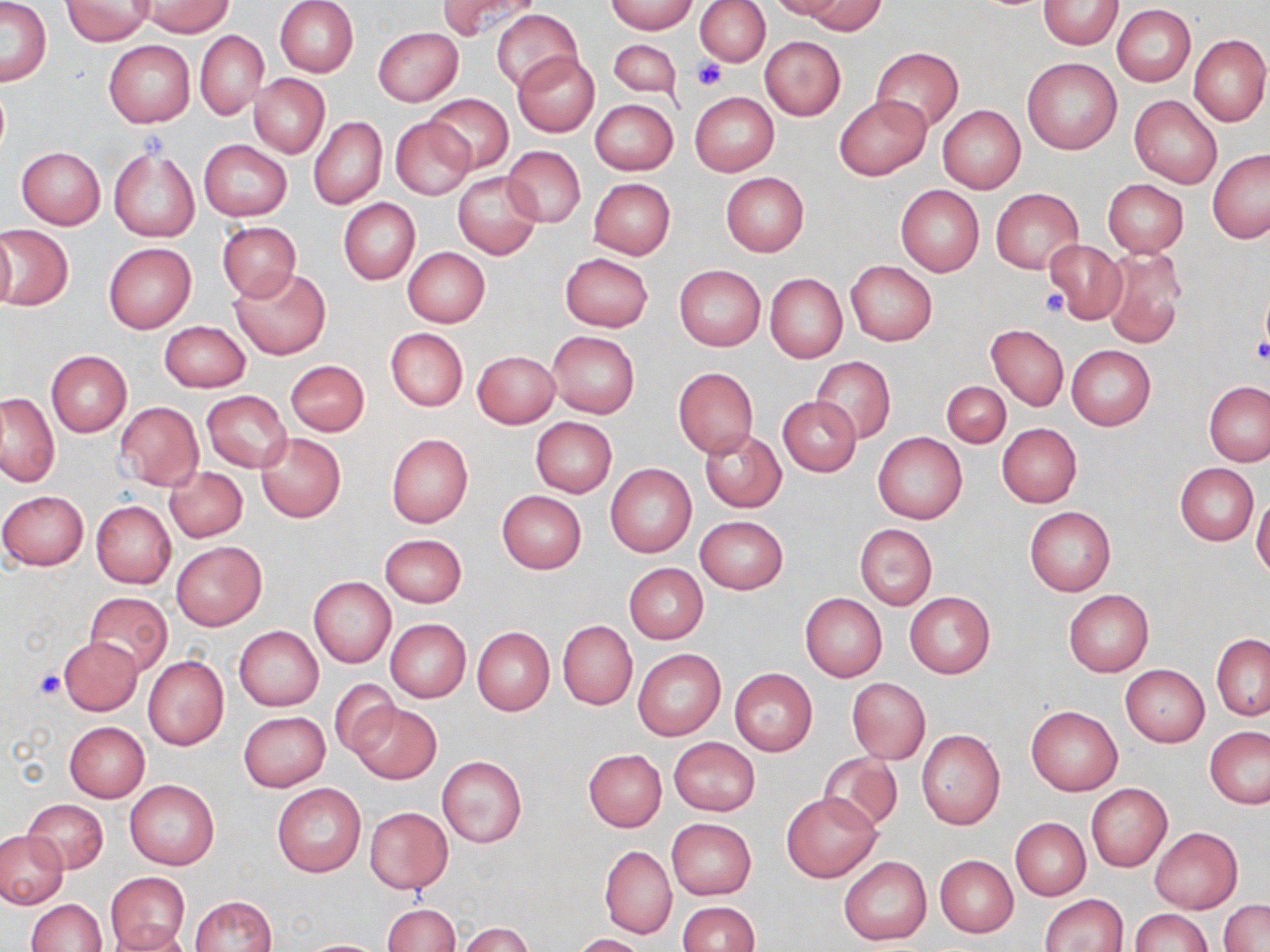

Approximate bounding boxes as (x1, y1, x2, y2) in pixels. Platelet locations: (693, 59, 728, 90), (1039, 289, 1069, 316), (1251, 337, 1270, 364), (36, 669, 65, 699). Uninfected red blood cell locations: (275, 0, 358, 77), (437, 0, 541, 40), (607, 0, 698, 34), (768, 0, 847, 19), (1039, 0, 1124, 49), (0, 1, 52, 86), (60, 1, 156, 45), (136, 1, 234, 37), (696, 1, 771, 66), (802, 1, 885, 35), (1112, 5, 1195, 86), (492, 9, 582, 93), (372, 27, 462, 107), (195, 30, 267, 119), (1188, 34, 1270, 127), (759, 36, 847, 121), (609, 39, 681, 98), (102, 40, 194, 128), (870, 47, 963, 133), (513, 51, 598, 136), (1022, 57, 1122, 155), (250, 74, 329, 157), (689, 91, 779, 176), (424, 94, 514, 173), (835, 95, 931, 180), (1129, 95, 1222, 188), (591, 99, 677, 175), (938, 106, 1025, 193), (310, 117, 387, 209), (391, 117, 475, 199), (198, 140, 292, 221), (16, 147, 105, 229), (503, 147, 585, 227), (109, 148, 199, 241), (1208, 150, 1270, 243), (452, 171, 542, 260), (721, 173, 808, 257), (588, 178, 675, 258), (1103, 179, 1188, 256), (896, 184, 984, 277), (990, 188, 1082, 272), (338, 198, 420, 285), (217, 220, 301, 301), (3, 225, 73, 312), (0, 226, 15, 312), (1043, 240, 1125, 322), (103, 242, 196, 332), (1101, 246, 1186, 348), (403, 247, 490, 328), (559, 252, 653, 331), (846, 262, 937, 346), (674, 265, 764, 350), (231, 267, 331, 359), (764, 273, 847, 362), (158, 320, 251, 391), (986, 323, 1068, 411), (385, 328, 468, 411), (547, 331, 640, 419), (1066, 345, 1156, 430), (46, 350, 132, 436), (471, 350, 560, 428), (812, 357, 896, 443), (285, 360, 370, 437), (673, 368, 758, 456), (941, 380, 1010, 448), (1204, 381, 1269, 467), (202, 391, 292, 472), (1, 392, 59, 486), (778, 396, 861, 475), (114, 401, 202, 490), (530, 417, 617, 497), (997, 423, 1081, 507), (700, 430, 786, 512), (256, 432, 346, 521), (872, 432, 967, 525), (385, 433, 473, 527), (606, 463, 697, 557), (1175, 464, 1258, 545), (165, 467, 247, 541), (0, 490, 89, 571), (497, 490, 587, 574), (1252, 493, 1270, 581), (91, 500, 175, 588), (1025, 506, 1115, 596), (695, 516, 789, 594), (855, 524, 936, 610), (379, 534, 467, 607), (172, 542, 265, 630), (623, 563, 708, 643), (309, 577, 395, 667), (1063, 589, 1153, 676), (905, 592, 995, 679), (800, 593, 886, 683), (84, 594, 173, 675), (385, 619, 470, 703), (558, 622, 636, 708), (234, 626, 324, 711), (472, 626, 554, 714), (1211, 634, 1270, 721), (57, 636, 141, 715), (632, 649, 725, 739), (143, 655, 229, 750), (1120, 664, 1209, 746), (729, 668, 818, 755), (846, 677, 930, 764), (329, 679, 401, 760), (350, 702, 440, 783), (1026, 706, 1121, 794), (239, 712, 329, 791), (64, 721, 150, 801), (1205, 727, 1270, 809), (916, 730, 1004, 830), (669, 737, 760, 816), (583, 748, 666, 831), (817, 753, 903, 832), (436, 755, 526, 848), (125, 780, 219, 868), (272, 783, 365, 877), (1086, 783, 1172, 871), (781, 791, 880, 882), (24, 799, 108, 872), (365, 807, 453, 893), (1011, 818, 1090, 901), (666, 819, 756, 899), (1150, 826, 1242, 913), (0, 831, 68, 909), (600, 845, 676, 939), (839, 855, 931, 946), (934, 855, 1018, 936), (106, 874, 190, 947), (1039, 893, 1128, 951), (189, 895, 277, 952), (25, 899, 107, 951), (1219, 900, 1270, 952), (677, 901, 759, 952), (382, 903, 460, 952), (1131, 909, 1212, 952), (458, 922, 533, 952), (105, 923, 194, 952), (573, 934, 647, 952), (300, 938, 388, 951). Slide-level diagnosis: no evidence of blood parasites. Captured at 1000x magnification. Optical microscopy. Thin blood film. May-Grünwald-Giemsa-stained preparation. Image is 1270×952 pixels. One field of a larger specimen.